Outline each blood parasite and name the species.
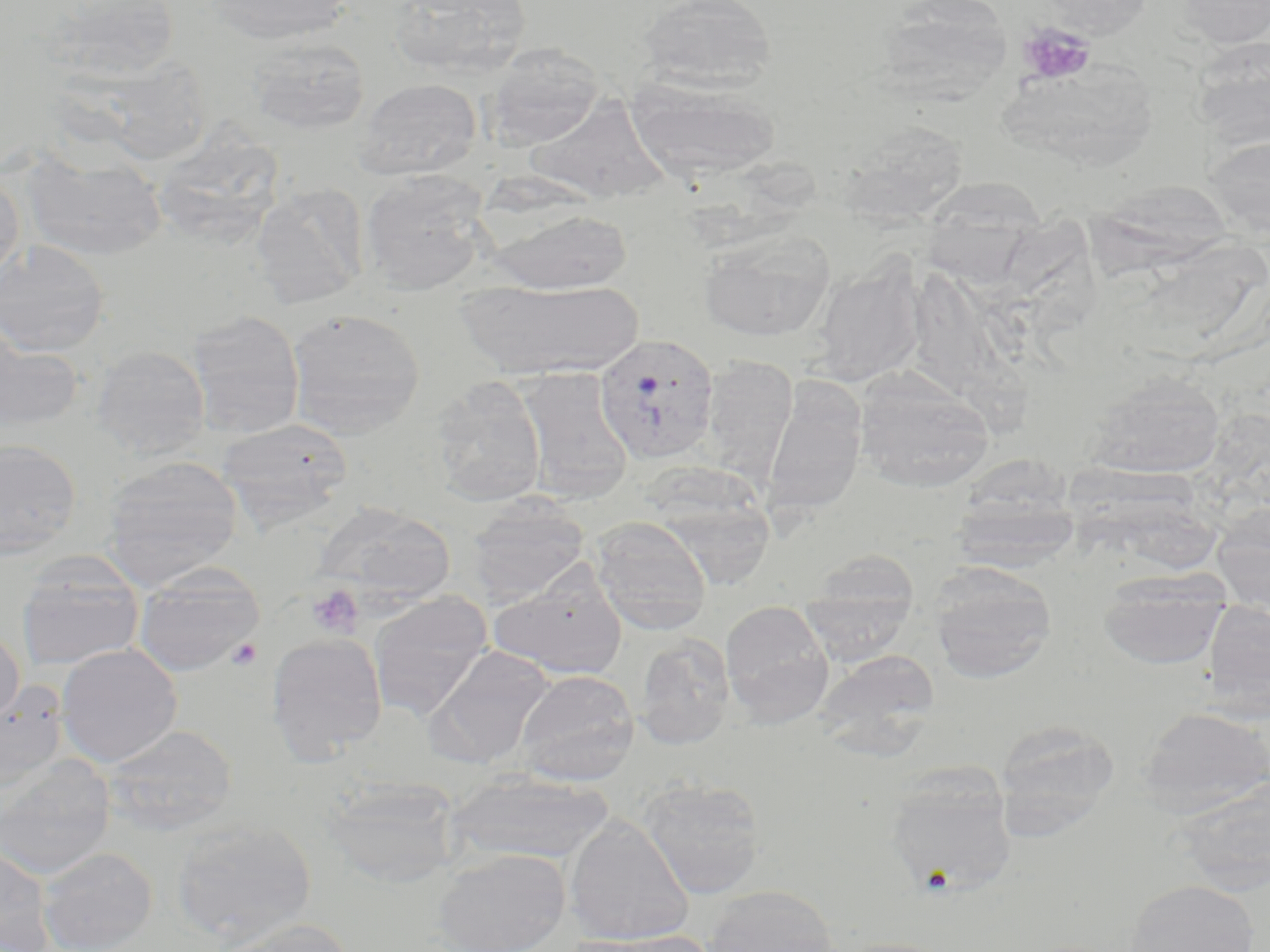
Approximate bounding boxes as [x1, y1, x2, y2] in pixels.
Plasmodium vivax-infected red blood cells: [593, 332, 720, 466].
No Plasmodium falciparum, Plasmodium ovale, Plasmodium malariae, Babesia divergens, or Trypanosoma brucei observed.

Summary:
  - Platelet locations: [1018, 22, 1097, 86], [306, 584, 364, 638], [227, 637, 262, 670]
  - Uninfected red blood cell locations: [35, 0, 181, 85], [206, 0, 352, 45], [389, 0, 531, 78], [637, 0, 777, 94], [1039, 0, 1153, 37], [1172, 0, 1270, 48], [874, 1, 1014, 105], [246, 36, 371, 136], [1191, 36, 1270, 149], [484, 43, 605, 151], [65, 60, 214, 164], [999, 60, 1158, 170], [354, 78, 482, 181], [627, 79, 781, 183], [523, 94, 671, 205], [162, 120, 285, 243], [836, 120, 969, 225], [1203, 135, 1270, 239], [21, 148, 168, 262], [0, 169, 25, 285], [359, 170, 493, 296], [917, 176, 1050, 281], [1090, 177, 1240, 276], [250, 182, 370, 309], [485, 208, 633, 294], [698, 228, 835, 342], [1147, 233, 1270, 365], [0, 240, 111, 358], [810, 258, 925, 386], [911, 258, 1033, 430], [456, 278, 645, 380], [286, 308, 426, 439], [188, 310, 305, 439], [0, 330, 86, 433], [92, 345, 211, 460], [701, 354, 798, 481], [516, 367, 634, 503], [854, 369, 994, 493], [1085, 371, 1226, 478], [430, 376, 546, 507], [762, 380, 867, 517], [216, 419, 353, 529], [0, 439, 82, 560], [101, 455, 244, 587], [1076, 461, 1233, 571], [642, 466, 778, 588], [948, 486, 1083, 573], [466, 496, 590, 605], [314, 503, 455, 604], [1211, 503, 1270, 612], [590, 517, 712, 634], [16, 553, 145, 671], [799, 557, 918, 665], [927, 563, 1057, 683], [132, 564, 265, 677], [489, 568, 628, 680], [1099, 571, 1229, 669], [367, 591, 493, 720], [720, 600, 834, 728], [1204, 601, 1269, 722], [0, 628, 24, 726], [266, 632, 388, 764], [633, 633, 736, 749], [55, 643, 183, 767], [426, 645, 555, 768], [815, 649, 940, 755], [514, 670, 640, 785], [0, 682, 69, 794], [1137, 706, 1270, 818], [992, 720, 1121, 840], [101, 724, 238, 836], [0, 754, 117, 880], [884, 769, 1018, 896], [443, 772, 613, 866], [320, 777, 461, 888], [1174, 777, 1270, 896], [639, 778, 766, 899], [564, 815, 695, 946], [169, 817, 317, 945], [0, 845, 55, 952], [37, 846, 158, 952], [433, 848, 570, 952], [1124, 879, 1260, 952], [701, 885, 841, 952], [212, 918, 354, 952], [571, 929, 716, 952]
  - Slide-level diagnosis: Plasmodium vivax
  - Field of view: one of a larger specimen
  - Preparation: thin blood smear
  - Image size: 1270×952 pixels
  - Magnification: 1000x
  - Stain: May-Grünwald-Giemsa
  - Modality: optical microscopy